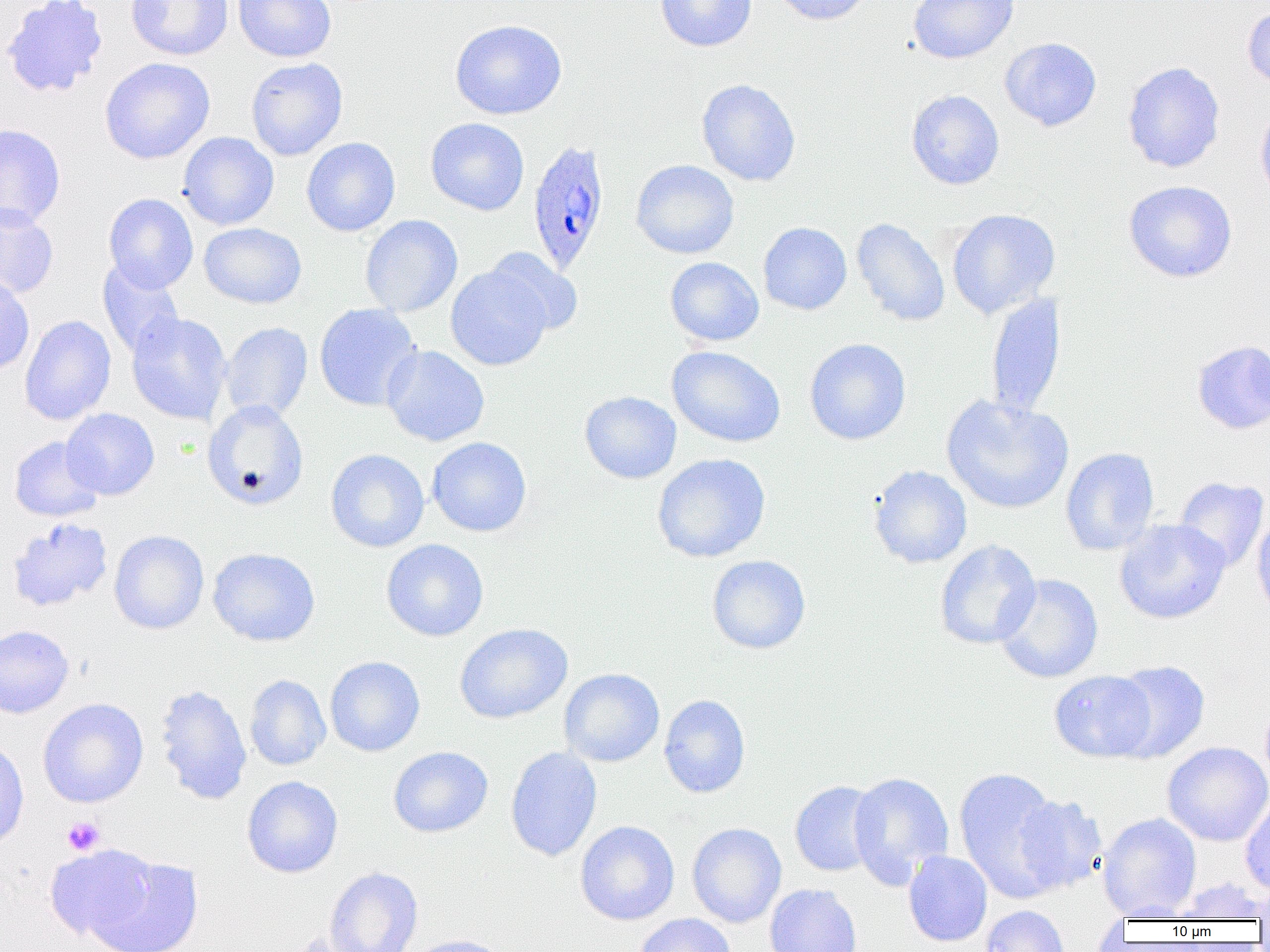

Summary:
  - Coordinate format: approximate bounding boxes as (x1, y1, x2, y2) in pixels
  - Uninfected red blood cell locations: (1, 0, 109, 99), (126, 0, 234, 61), (655, 0, 757, 52), (769, 0, 874, 25), (908, 0, 1019, 64), (233, 1, 336, 63), (1242, 4, 1270, 93), (449, 18, 567, 120), (999, 37, 1102, 131), (100, 57, 215, 164), (246, 58, 348, 160), (1122, 61, 1225, 173), (696, 78, 801, 187), (906, 90, 1005, 190), (1254, 100, 1270, 205), (425, 117, 530, 216), (0, 123, 66, 230), (178, 132, 279, 230), (301, 137, 401, 237), (631, 159, 739, 259), (1123, 180, 1237, 283), (103, 193, 199, 293), (0, 204, 59, 300), (946, 208, 1060, 319), (360, 215, 462, 317), (851, 217, 950, 328), (199, 222, 307, 309), (758, 222, 852, 315), (484, 248, 583, 336), (665, 256, 765, 347), (98, 259, 184, 360), (445, 262, 553, 371), (0, 274, 34, 377), (985, 293, 1066, 419), (314, 303, 421, 411), (126, 312, 232, 425), (19, 315, 117, 426), (220, 322, 313, 423), (804, 338, 911, 445), (1191, 340, 1270, 434), (381, 344, 490, 447), (667, 346, 786, 447), (579, 390, 682, 484), (940, 394, 1074, 514), (202, 400, 309, 511), (61, 408, 160, 500), (9, 435, 105, 522), (426, 437, 532, 537), (1060, 446, 1159, 556), (326, 449, 429, 552), (651, 453, 771, 562), (868, 465, 972, 568), (1173, 476, 1269, 572), (1251, 511, 1270, 622), (6, 518, 113, 612), (1114, 519, 1231, 624), (109, 530, 209, 634), (381, 539, 489, 641), (934, 539, 1041, 649), (208, 547, 320, 647), (706, 554, 811, 654), (994, 573, 1104, 683), (454, 622, 573, 724), (0, 625, 74, 718), (325, 655, 425, 757), (1107, 660, 1210, 763), (558, 668, 665, 767), (1049, 670, 1157, 762), (244, 674, 331, 770), (153, 684, 252, 806), (658, 694, 751, 798), (1260, 695, 1270, 792), (37, 698, 148, 808), (0, 738, 29, 851), (1162, 741, 1270, 846), (387, 746, 493, 838), (505, 746, 602, 861), (954, 766, 1065, 900), (848, 771, 954, 888), (241, 775, 343, 878), (789, 781, 884, 876), (1012, 794, 1108, 894), (1240, 794, 1270, 897), (1097, 813, 1202, 921), (575, 820, 680, 925), (687, 822, 787, 928), (44, 843, 158, 944), (79, 850, 203, 952), (903, 851, 992, 946), (323, 866, 424, 952), (1170, 877, 1268, 922), (1253, 878, 1270, 924), (764, 883, 863, 952), (980, 905, 1069, 952), (634, 913, 737, 952), (281, 929, 377, 952), (401, 934, 516, 952)
  - Platelet locations: (62, 816, 105, 855)
  - Plasmodium ovale-infected red blood cell locations: (527, 139, 611, 275)
  - Slide-level diagnosis: Plasmodium ovale
  - Magnification: 1000x
  - Preparation: thin blood film
  - Image size: 1270×952 pixels
  - Modality: light microscopy
  - Field of view: single